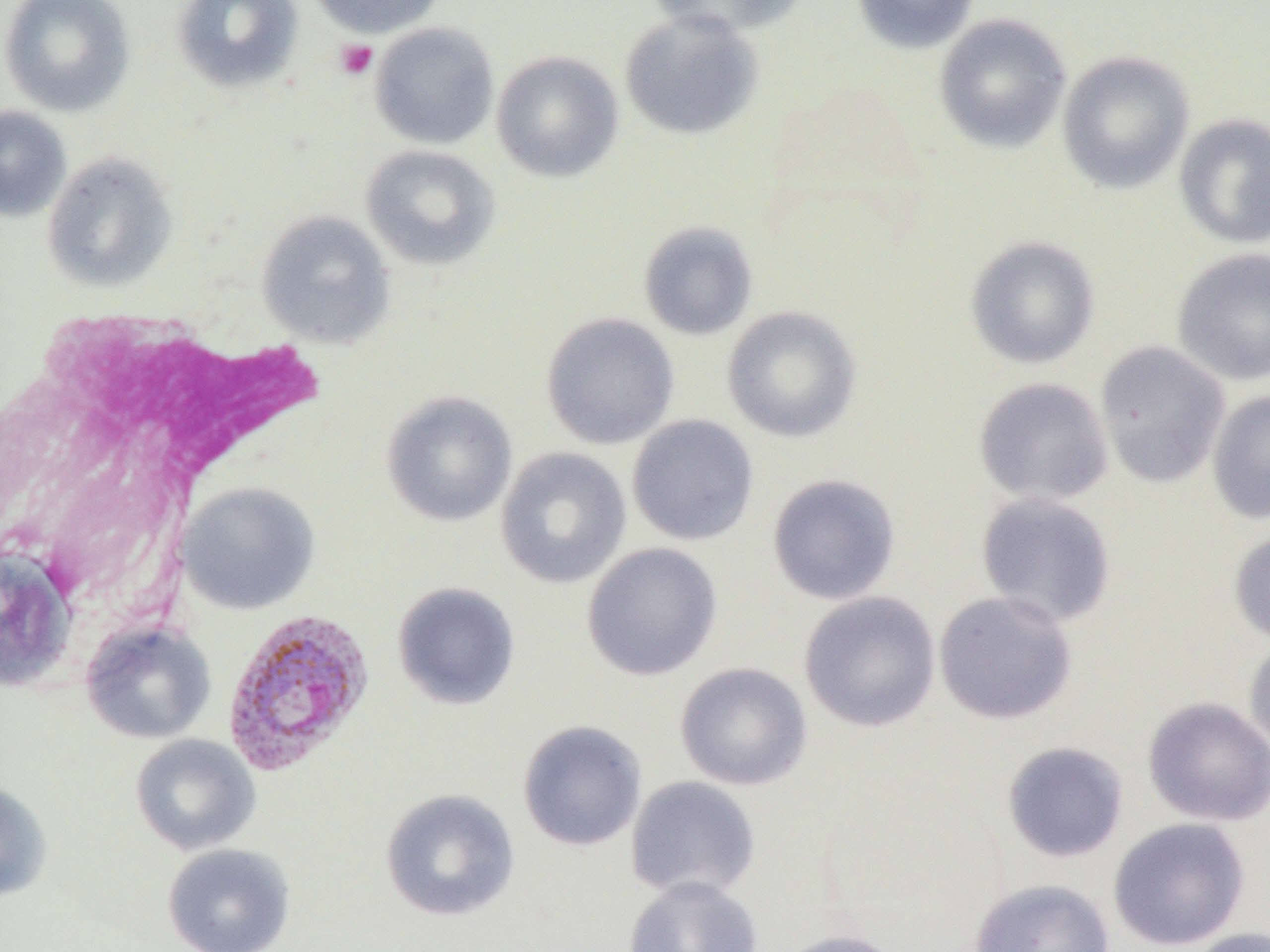 Approximate bounding boxes as [x1, y1, x2, y2] in pixels. Platelet locations: [335, 39, 377, 79]. Plasmodium vivax-infected red blood cell locations: [221, 607, 375, 776]. White blood cell locations: [11, 302, 335, 629]. Uninfected red blood cell locations: [0, 0, 136, 117], [171, 0, 305, 94], [305, 0, 445, 39], [647, 0, 806, 38], [852, 0, 980, 54], [619, 9, 763, 141], [933, 13, 1072, 153], [369, 22, 500, 149], [1056, 50, 1195, 195], [491, 51, 624, 183], [0, 106, 71, 222], [1174, 112, 1270, 249], [360, 145, 501, 271], [41, 151, 178, 292], [255, 210, 396, 348], [638, 221, 758, 340], [965, 236, 1100, 369], [1170, 247, 1270, 387], [721, 306, 862, 442], [541, 313, 680, 450], [1094, 341, 1230, 488], [973, 377, 1114, 506], [1207, 389, 1270, 524], [381, 391, 517, 527], [627, 414, 759, 546], [494, 447, 632, 589], [767, 473, 901, 605], [178, 482, 320, 614], [975, 492, 1117, 628], [1228, 526, 1270, 645], [581, 542, 723, 681], [0, 549, 75, 692], [391, 582, 521, 711], [933, 590, 1078, 725], [798, 591, 941, 733], [81, 620, 216, 744], [1244, 635, 1270, 757], [674, 661, 813, 791], [1142, 696, 1270, 827], [517, 720, 648, 852], [130, 734, 261, 855], [1001, 741, 1129, 863], [625, 776, 762, 902], [0, 779, 53, 903], [379, 789, 520, 922], [1108, 816, 1250, 951], [162, 843, 296, 952], [623, 875, 764, 952], [968, 879, 1115, 952], [1181, 927, 1270, 952], [776, 928, 907, 952]. Slide-level diagnosis: Plasmodium vivax. 1000x magnification. Thin blood smear. One field of a larger specimen. Image is 1270×952 pixels. Light microscopy.